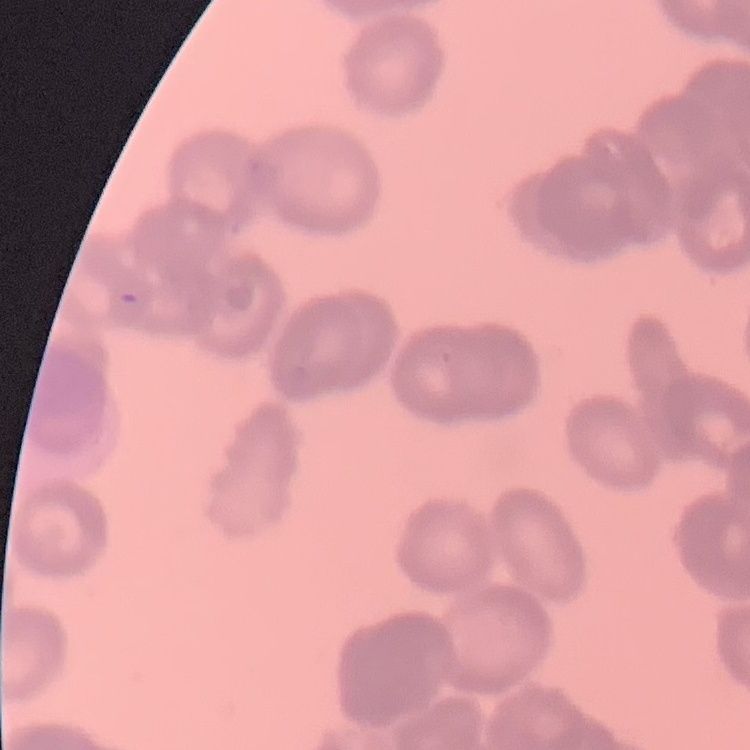
The erythrocytes exhibit rouleaux formation. Thin blood film. Stained with either Field's or Giemsa. One tile cut from a larger photomicrograph.